Comment on the morphology of the red blood cells.
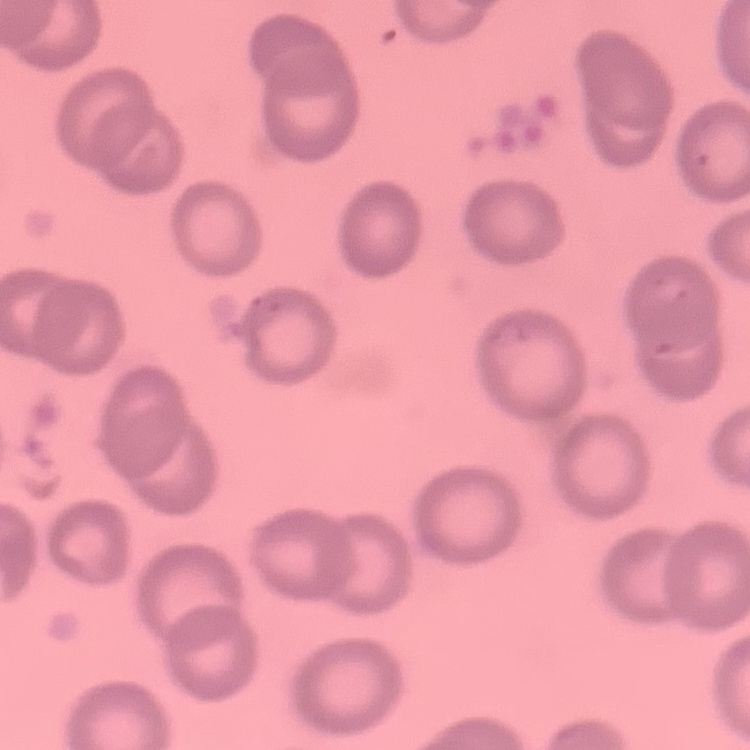

No rouleaux formation.

preparation: thin blood film
stain: Field's or Giemsa
image_type: square crop of a larger photomicrograph